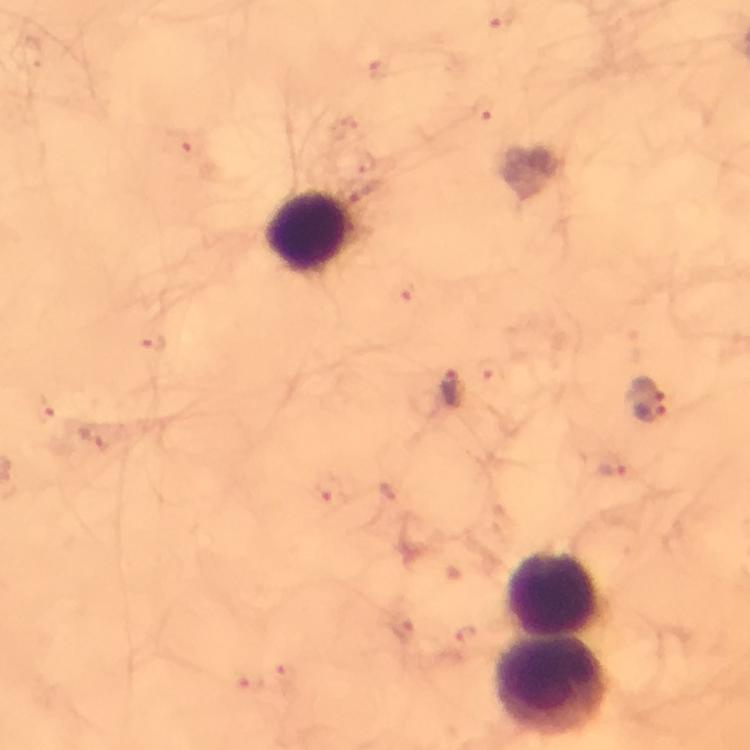

Approximate centers as [x, y] in pixels.
Summary:
  - Plasmodium parasite locations: [501, 22], [483, 109], [184, 144], [401, 294], [155, 344], [453, 389], [643, 389], [651, 410], [44, 411], [614, 471], [325, 493], [464, 636]
  - Leukocyte locations: [309, 232], [553, 594], [554, 688]
  - Preparation: thick blood smear
  - Magnification: 100x
  - Image size: 750×750 pixels
  - Cropped from: one field of view
  - Capture: smartphone camera through the microscope
  - Stain: Giemsa
  - Immersion oil: applied
  - Context: from a malaria diagnostic workup